Comment on the morphology of the red blood cells.
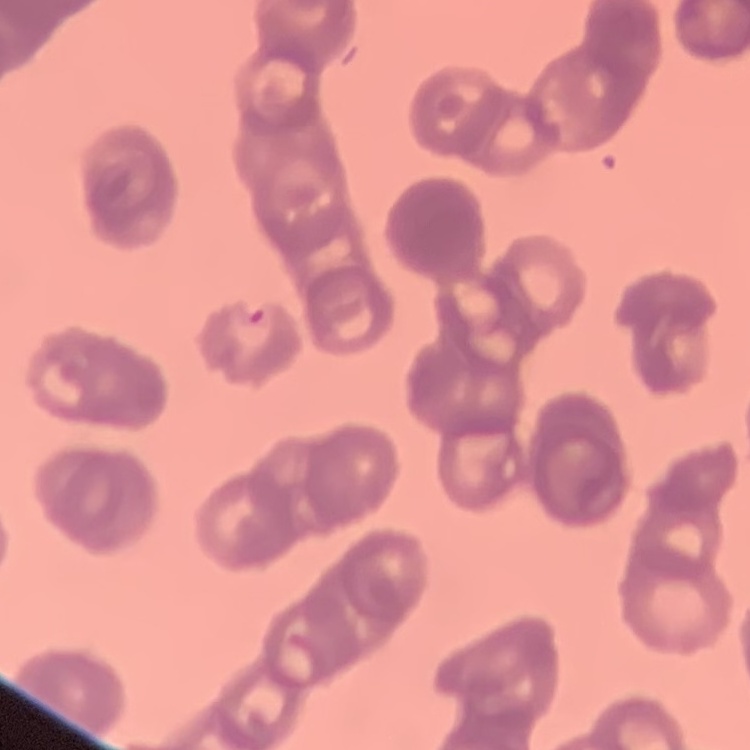
They show rouleaux formation.

Summary:
  - Preparation: thin blood film
  - Image type: square crop of a larger photomicrograph
  - Stain: Field's or Giemsa